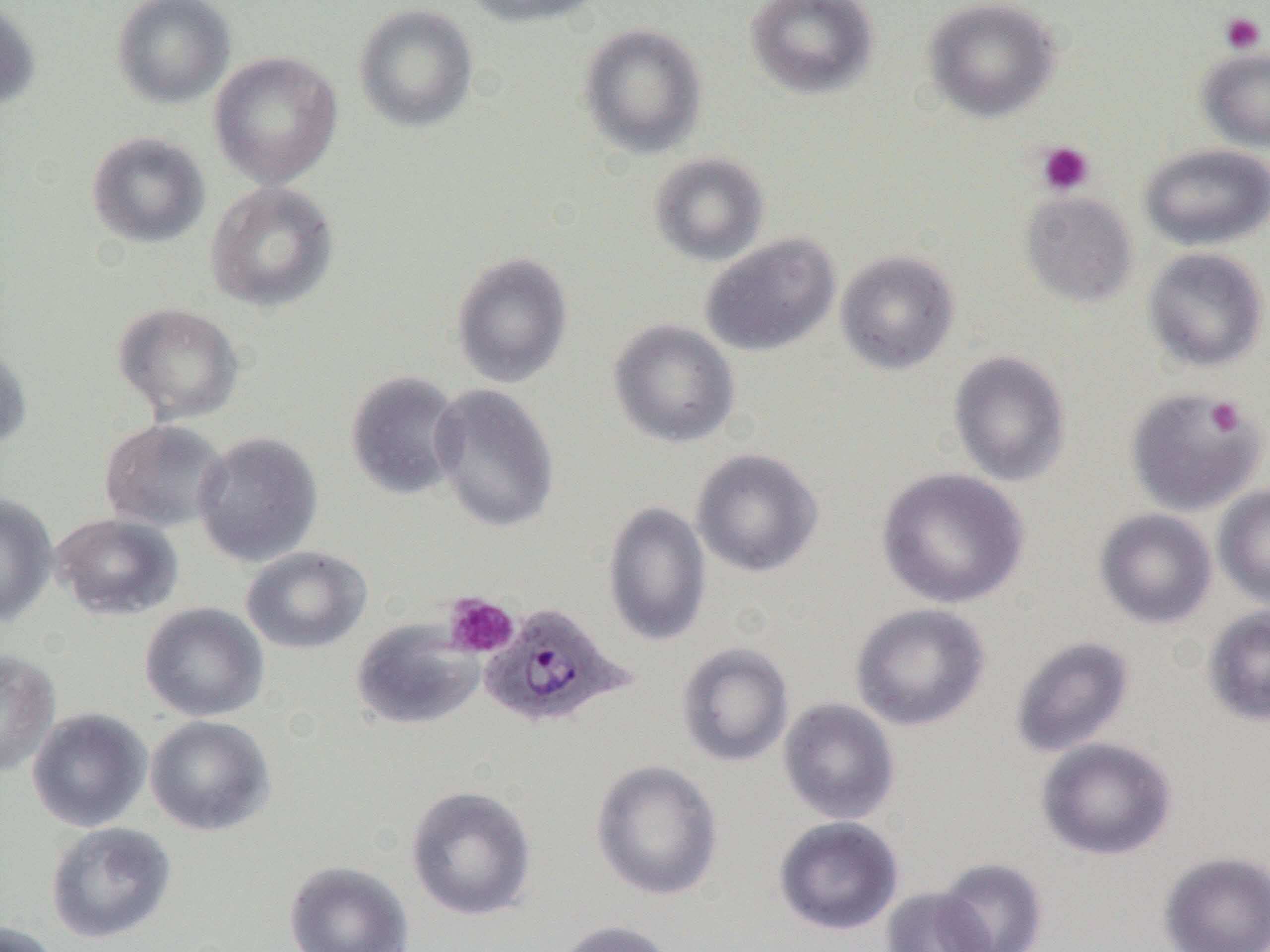
Summary:
  - Coordinate format: approximate bounding boxes as named x1/y1/x2/y2 corners in pixels
  - Plasmodium ovale-infected red blood cell locations: (x1=479, y1=603, x2=632, y2=730)
  - Uninfected red blood cell locations: (x1=111, y1=0, x2=235, y2=109), (x1=462, y1=0, x2=605, y2=28), (x1=744, y1=0, x2=879, y2=100), (x1=922, y1=0, x2=1061, y2=122), (x1=0, y1=1, x2=42, y2=111), (x1=353, y1=3, x2=479, y2=133), (x1=578, y1=22, x2=708, y2=158), (x1=1196, y1=47, x2=1270, y2=152), (x1=208, y1=50, x2=343, y2=189), (x1=86, y1=131, x2=211, y2=249), (x1=1139, y1=143, x2=1270, y2=250), (x1=648, y1=152, x2=769, y2=266), (x1=205, y1=181, x2=340, y2=314), (x1=1020, y1=192, x2=1138, y2=307), (x1=700, y1=233, x2=840, y2=357), (x1=1142, y1=247, x2=1268, y2=373), (x1=835, y1=250, x2=960, y2=375), (x1=451, y1=251, x2=573, y2=388), (x1=112, y1=302, x2=244, y2=425), (x1=608, y1=319, x2=740, y2=449), (x1=0, y1=341, x2=33, y2=451), (x1=948, y1=350, x2=1071, y2=486), (x1=345, y1=371, x2=466, y2=500), (x1=429, y1=383, x2=560, y2=534), (x1=1125, y1=386, x2=1265, y2=515), (x1=99, y1=419, x2=231, y2=533), (x1=192, y1=431, x2=324, y2=567), (x1=690, y1=448, x2=824, y2=577), (x1=876, y1=466, x2=1028, y2=609), (x1=1213, y1=484, x2=1270, y2=609), (x1=0, y1=492, x2=58, y2=627), (x1=602, y1=501, x2=712, y2=646), (x1=1094, y1=508, x2=1217, y2=629), (x1=50, y1=512, x2=183, y2=620), (x1=241, y1=545, x2=372, y2=655), (x1=140, y1=602, x2=269, y2=722), (x1=850, y1=602, x2=991, y2=730), (x1=1202, y1=606, x2=1270, y2=727), (x1=351, y1=617, x2=484, y2=730), (x1=1010, y1=636, x2=1135, y2=758), (x1=676, y1=642, x2=794, y2=766), (x1=0, y1=649, x2=61, y2=778), (x1=778, y1=697, x2=900, y2=825), (x1=27, y1=708, x2=151, y2=833), (x1=145, y1=715, x2=275, y2=837), (x1=1036, y1=737, x2=1177, y2=861), (x1=590, y1=759, x2=724, y2=901), (x1=405, y1=784, x2=537, y2=922), (x1=772, y1=816, x2=904, y2=936), (x1=45, y1=821, x2=176, y2=944), (x1=1158, y1=851, x2=1270, y2=952), (x1=936, y1=857, x2=1049, y2=952), (x1=284, y1=860, x2=414, y2=952), (x1=880, y1=886, x2=997, y2=952), (x1=553, y1=919, x2=679, y2=952), (x1=0, y1=920, x2=60, y2=952)
  - Platelet locations: (x1=1219, y1=12, x2=1266, y2=54), (x1=1036, y1=141, x2=1094, y2=196), (x1=1205, y1=397, x2=1246, y2=436), (x1=444, y1=593, x2=519, y2=658)
  - Slide-level diagnosis: Plasmodium ovale
  - Preparation: thin blood film
  - Field of view: single
  - Modality: light microscopy
  - Magnification: 1000x
  - Image size: 1270×952 pixels